State which parasite is depicted.
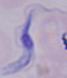

This is a trypanosome.

Summary:
  - Magnification: 1000x
  - Modality: photomicrograph